Name the parasite shown.
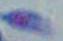
This is Toxoplasma gondii.

modality = photomicrograph
magnification = 1000x